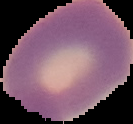
From a thin blood smear. Segmented cell region on a black background. Result: no Plasmodium parasites detected. Image is 133×124 pixels.